Outline each uninfected red blood cell.
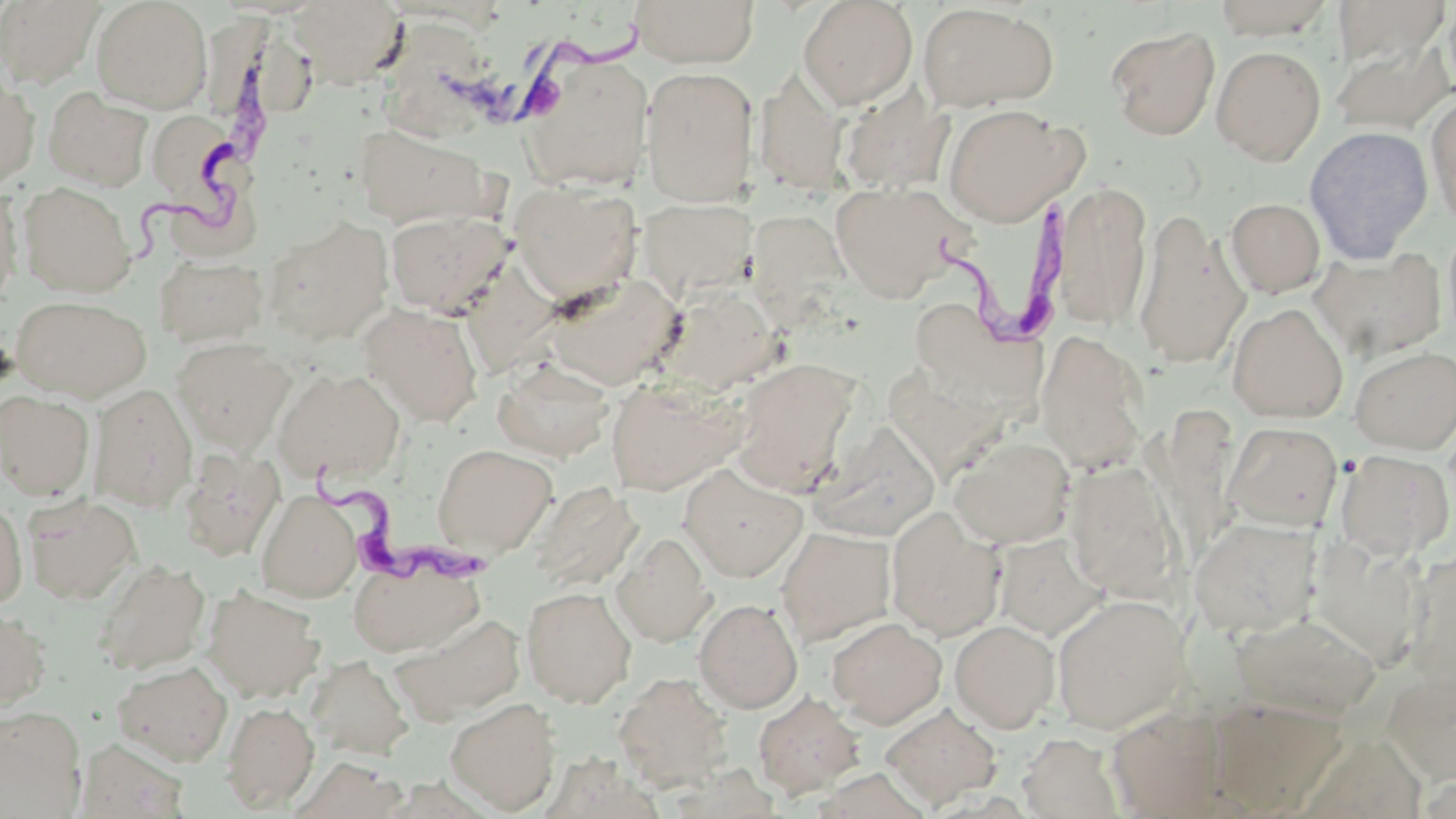
Approximate bounding boxes as named x1/y1/x2/y2 corners in pixels.
Uninfected red blood cells: (x1=0, y1=0, x2=104, y2=88), (x1=91, y1=0, x2=211, y2=113), (x1=289, y1=0, x2=406, y2=88), (x1=631, y1=0, x2=760, y2=68), (x1=798, y1=0, x2=918, y2=110), (x1=1210, y1=0, x2=1339, y2=39), (x1=1332, y1=1, x2=1450, y2=70), (x1=917, y1=4, x2=1059, y2=112), (x1=385, y1=19, x2=489, y2=144), (x1=1107, y1=26, x2=1220, y2=140), (x1=1330, y1=32, x2=1454, y2=136), (x1=1212, y1=45, x2=1326, y2=165), (x1=518, y1=54, x2=654, y2=192), (x1=640, y1=67, x2=757, y2=207), (x1=753, y1=73, x2=848, y2=195), (x1=0, y1=75, x2=40, y2=191), (x1=43, y1=87, x2=154, y2=191), (x1=838, y1=88, x2=955, y2=194), (x1=1425, y1=92, x2=1456, y2=229), (x1=942, y1=104, x2=1082, y2=226), (x1=144, y1=106, x2=246, y2=213), (x1=351, y1=123, x2=495, y2=230), (x1=1304, y1=126, x2=1433, y2=264), (x1=831, y1=181, x2=968, y2=301), (x1=511, y1=182, x2=641, y2=303), (x1=1053, y1=182, x2=1152, y2=330), (x1=18, y1=183, x2=135, y2=297), (x1=0, y1=187, x2=22, y2=311), (x1=1225, y1=197, x2=1325, y2=297), (x1=637, y1=198, x2=756, y2=303), (x1=744, y1=207, x2=857, y2=326), (x1=1132, y1=208, x2=1251, y2=370), (x1=385, y1=209, x2=513, y2=316), (x1=263, y1=216, x2=393, y2=345), (x1=1442, y1=221, x2=1456, y2=347), (x1=1310, y1=247, x2=1447, y2=361), (x1=154, y1=255, x2=267, y2=345), (x1=545, y1=273, x2=687, y2=389), (x1=658, y1=285, x2=783, y2=394), (x1=11, y1=296, x2=151, y2=401), (x1=360, y1=303, x2=484, y2=426), (x1=1227, y1=303, x2=1348, y2=422), (x1=913, y1=312, x2=1051, y2=401), (x1=1036, y1=330, x2=1150, y2=474), (x1=172, y1=339, x2=293, y2=452), (x1=1349, y1=346, x2=1456, y2=454), (x1=492, y1=358, x2=615, y2=462), (x1=730, y1=358, x2=861, y2=492), (x1=274, y1=368, x2=405, y2=483), (x1=887, y1=369, x2=1004, y2=482), (x1=607, y1=377, x2=745, y2=496), (x1=91, y1=384, x2=197, y2=510), (x1=0, y1=391, x2=95, y2=499), (x1=1224, y1=422, x2=1342, y2=531), (x1=809, y1=423, x2=941, y2=542), (x1=949, y1=435, x2=1075, y2=548), (x1=433, y1=443, x2=557, y2=557), (x1=178, y1=446, x2=284, y2=561), (x1=1334, y1=449, x2=1455, y2=559), (x1=1063, y1=461, x2=1184, y2=602), (x1=679, y1=464, x2=807, y2=582), (x1=531, y1=480, x2=643, y2=592), (x1=256, y1=490, x2=362, y2=602), (x1=23, y1=495, x2=140, y2=605), (x1=0, y1=498, x2=28, y2=609), (x1=886, y1=508, x2=1004, y2=640), (x1=1190, y1=516, x2=1322, y2=637), (x1=777, y1=526, x2=895, y2=646), (x1=613, y1=532, x2=715, y2=646), (x1=993, y1=534, x2=1105, y2=640), (x1=348, y1=558, x2=483, y2=657), (x1=94, y1=559, x2=211, y2=674), (x1=202, y1=586, x2=324, y2=702), (x1=521, y1=586, x2=636, y2=707), (x1=1051, y1=594, x2=1190, y2=734), (x1=694, y1=599, x2=803, y2=713), (x1=0, y1=607, x2=52, y2=713), (x1=1230, y1=609, x2=1381, y2=720), (x1=390, y1=612, x2=526, y2=723), (x1=827, y1=617, x2=947, y2=728), (x1=950, y1=619, x2=1059, y2=733), (x1=306, y1=654, x2=413, y2=760), (x1=113, y1=660, x2=233, y2=766), (x1=1384, y1=667, x2=1455, y2=787), (x1=614, y1=672, x2=732, y2=792), (x1=753, y1=691, x2=865, y2=800), (x1=1206, y1=696, x2=1345, y2=815), (x1=445, y1=697, x2=561, y2=814), (x1=221, y1=701, x2=319, y2=813), (x1=880, y1=704, x2=1002, y2=809), (x1=0, y1=705, x2=87, y2=818), (x1=1106, y1=705, x2=1231, y2=817), (x1=1016, y1=732, x2=1124, y2=817), (x1=77, y1=738, x2=190, y2=818), (x1=296, y1=757, x2=409, y2=818).

Summary:
  - Trypanosoma brucei locations: (x1=454, y1=21, x2=657, y2=132), (x1=114, y1=38, x2=291, y2=263), (x1=924, y1=198, x2=1086, y2=349), (x1=311, y1=451, x2=487, y2=596)
  - Slide-level diagnosis: Trypanosoma brucei
  - Modality: light microscopy
  - Field of view: one of a larger specimen
  - Image size: 1456×819 pixels
  - Magnification: 1000x
  - Preparation: thin blood film
  - Stain: May-Grünwald-Giemsa